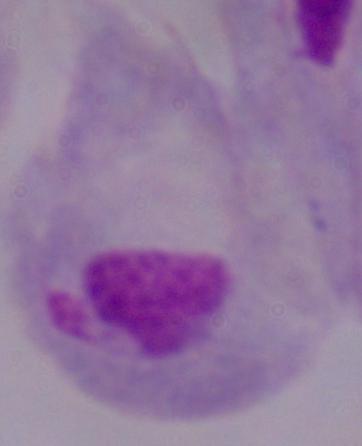

Summary:
  - Magnification: 1000x
  - Modality: micrograph
  - Identification: trichomonad